Name the parasite shown.
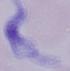

This is a trypanosome.

Summary:
  - Magnification: 1000x
  - Modality: photomicrograph